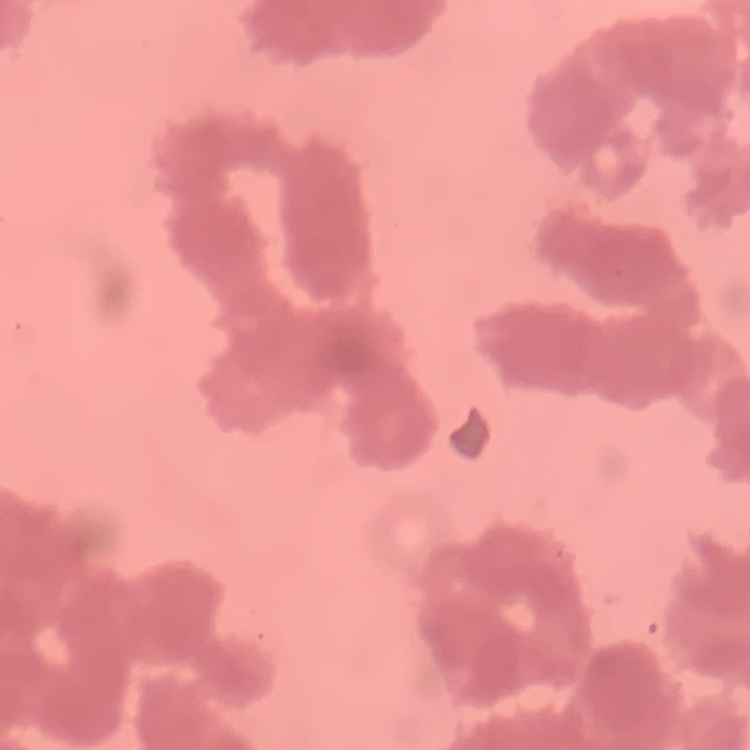

The erythrocytes show rouleaux formation. Thin blood smear. One tile cut from a larger photomicrograph. Field's or Giemsa stain.